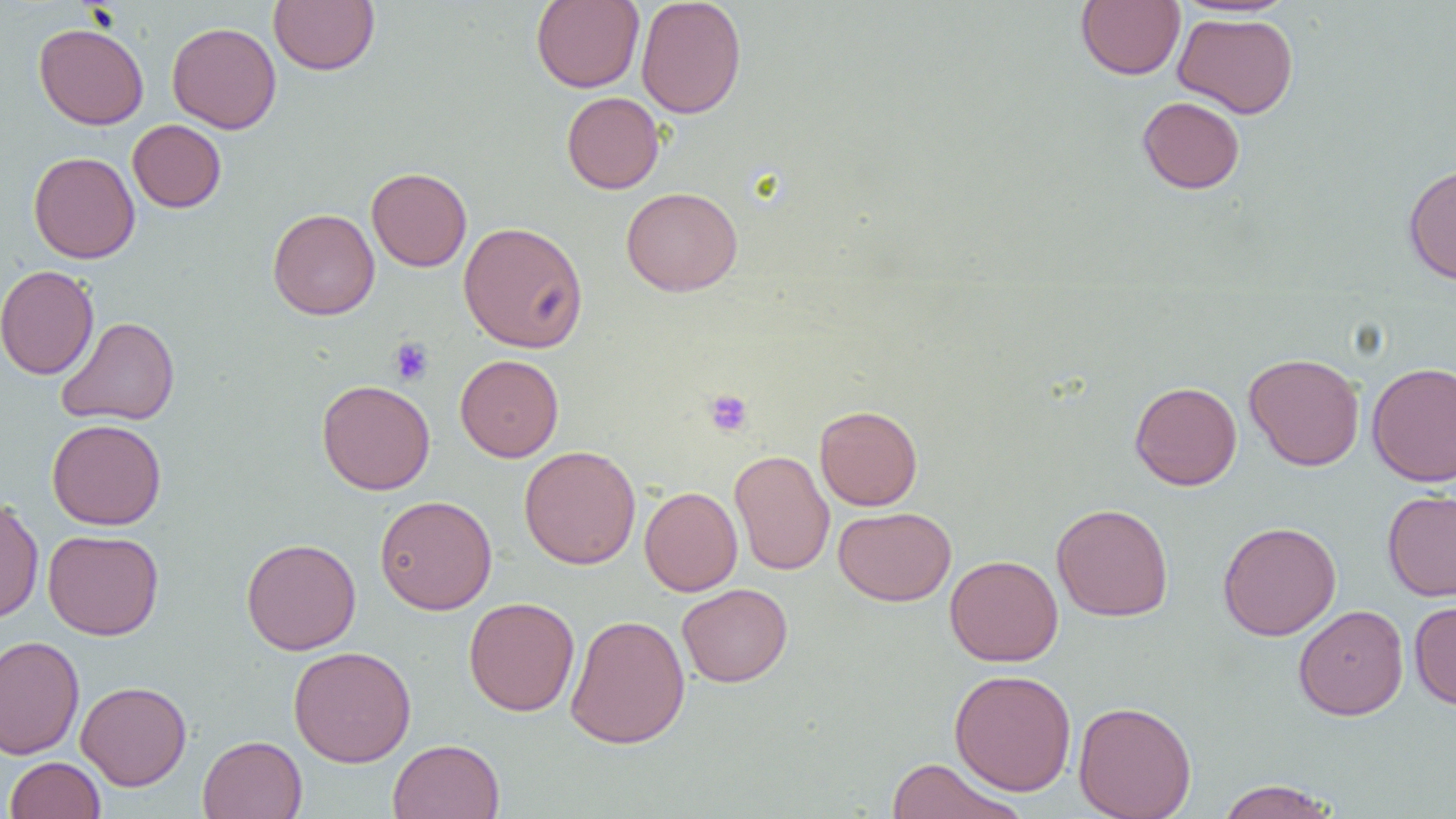
slide_level_diagnosis: negative for blood parasites
uninfected_red_blood_cell_locations: 'approximate bounding boxes as (x1, y1, x2, y2) in pixels: (269, 0, 379, 75), (531, 0, 644, 93), (635, 0, 747, 119), (1076, 1, 1185, 80), (1173, 12, 1298, 119), (33, 22, 149, 130), (167, 22, 281, 134), (561, 91, 664, 194), (1137, 96, 1245, 194), (127, 119, 226, 213), (28, 151, 140, 263), (1403, 164, 1456, 285), (366, 167, 472, 272), (621, 187, 743, 296), (267, 208, 379, 320), (458, 221, 588, 353), (0, 265, 99, 380), (56, 316, 180, 426), (1244, 352, 1365, 471), (455, 354, 564, 462), (1367, 362, 1456, 487), (317, 379, 435, 495), (1129, 381, 1243, 490), (815, 405, 922, 511), (47, 418, 166, 530), (519, 445, 641, 569), (730, 449, 834, 576), (640, 486, 743, 596), (1382, 489, 1456, 602), (375, 495, 497, 615), (0, 497, 44, 623), (1051, 503, 1174, 622), (834, 507, 956, 606), (1217, 521, 1341, 640), (43, 529, 164, 640), (241, 537, 361, 655), (944, 554, 1063, 666), (677, 583, 793, 687), (463, 597, 579, 716), (1408, 600, 1456, 710), (1293, 605, 1408, 721), (565, 613, 690, 749), (0, 635, 85, 760), (288, 646, 416, 767), (949, 668, 1077, 796), (76, 680, 191, 791), (1073, 700, 1197, 819), (198, 735, 307, 819), (388, 739, 504, 819), (4, 756, 106, 819), (885, 758, 1027, 818), (1214, 779, 1340, 819)'
image_size: 1456×819 pixels
preparation: thin blood film
platelet_locations: 'approximate bounding boxes as (x1, y1, x2, y2) in pixels: (389, 337, 435, 386), (704, 389, 753, 436)'
field_of_view: single
magnification: 1000x
modality: light microscopy